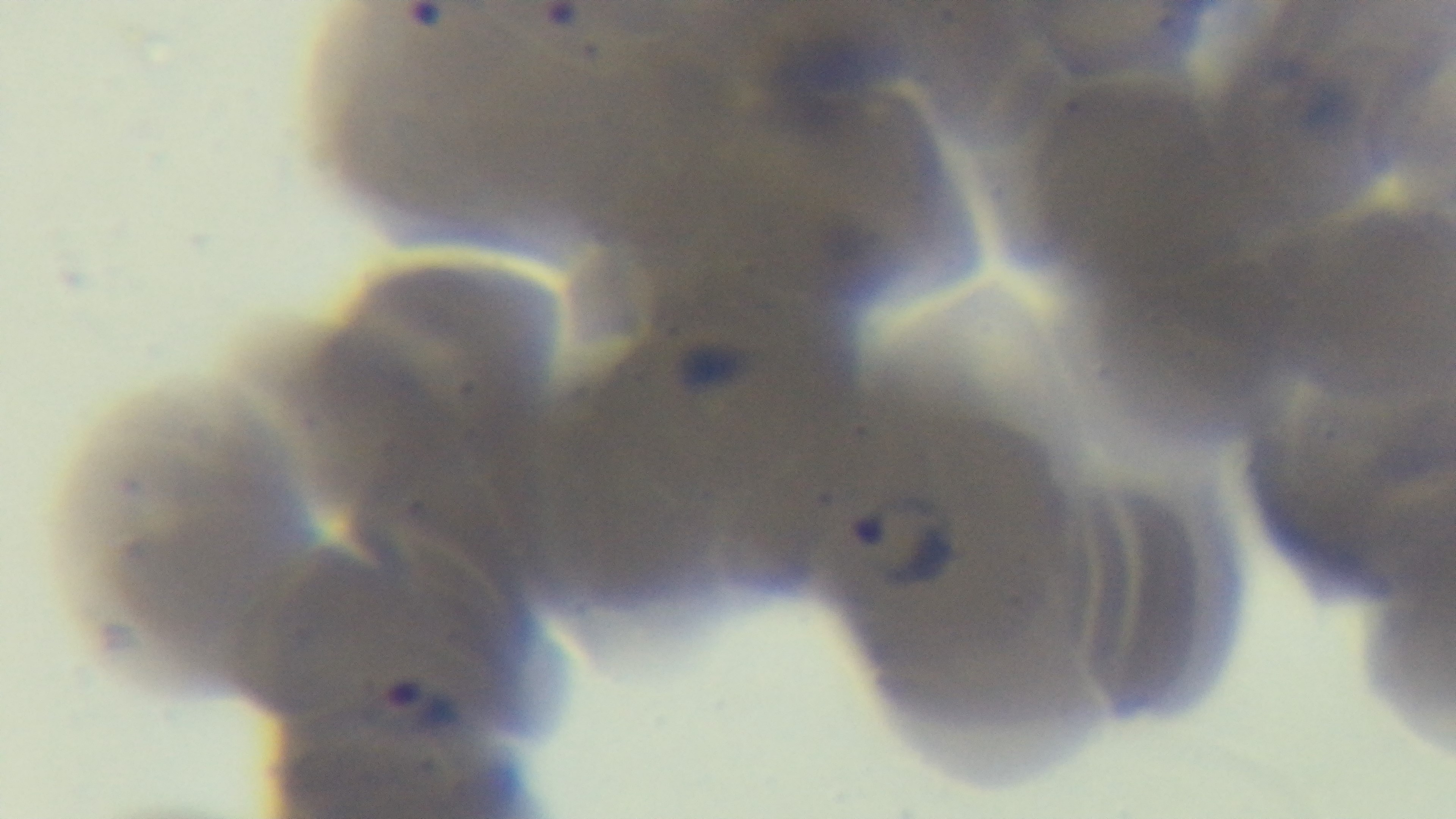
Summary:
  - Malaria status: infected
  - Modality: light microscopy
  - Field of view: one from the slide
  - Preparation: thin blood film
  - Objective: 100x oil immersion
  - Stain: Giemsa
  - Capture: mounted 4K digital camera